Locate and identify every blood parasite.
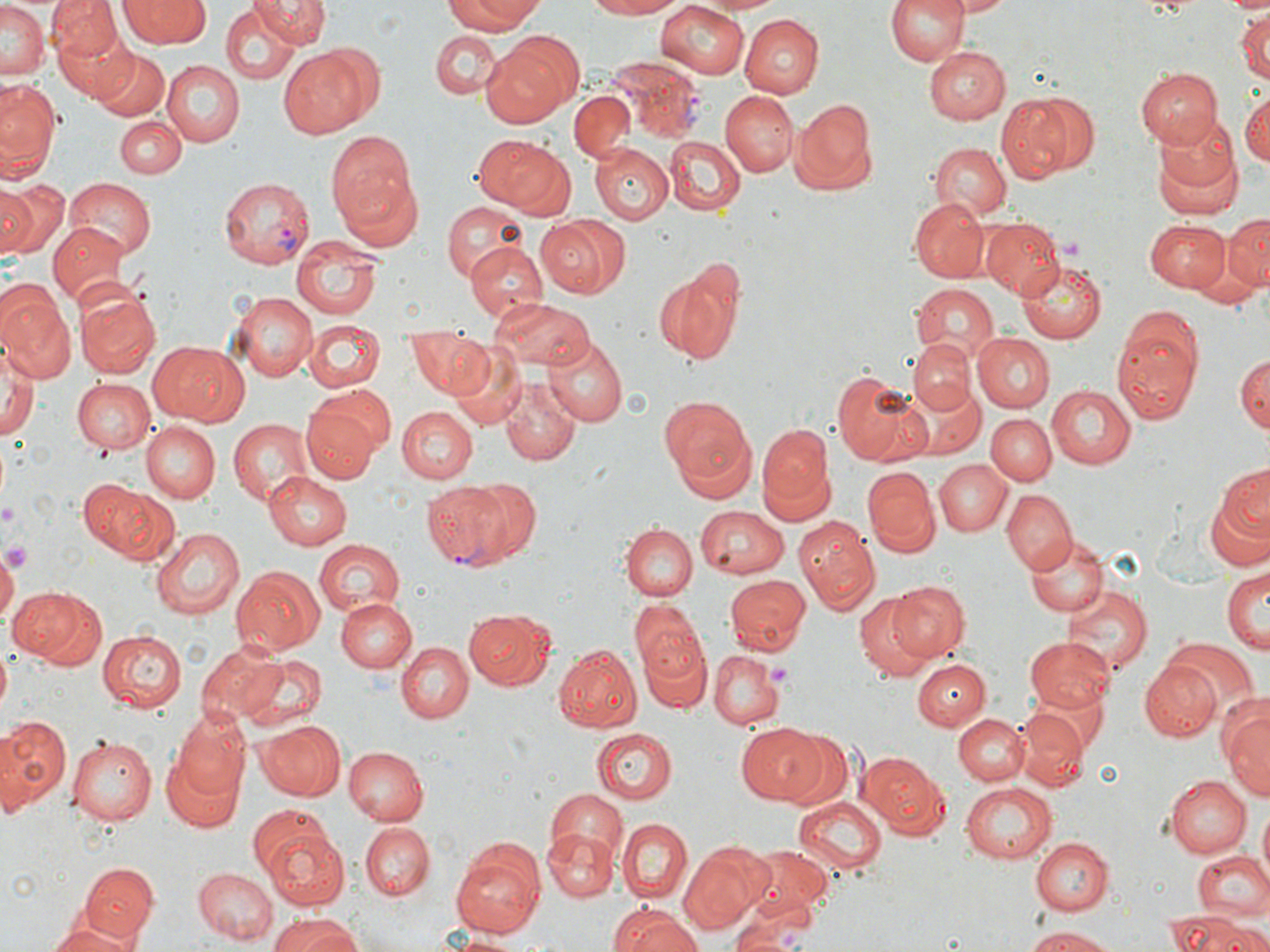

Approximate bounding boxes as named x1/y1/x2/y2 corners in pixels.
Plasmodium vivax-infected red blood cells: (x1=609, y1=55, x2=705, y2=139), (x1=217, y1=176, x2=315, y2=266), (x1=423, y1=479, x2=516, y2=568).
No Plasmodium falciparum, Plasmodium ovale, Plasmodium malariae, Babesia divergens, or Trypanosoma brucei observed.

Summary:
  - Platelet locations: (x1=1056, y1=234, x2=1084, y2=262), (x1=766, y1=663, x2=791, y2=688)
  - Uninfected red blood cell locations: (x1=49, y1=0, x2=125, y2=66), (x1=257, y1=0, x2=328, y2=46), (x1=445, y1=0, x2=544, y2=34), (x1=584, y1=0, x2=686, y2=20), (x1=886, y1=0, x2=969, y2=67), (x1=949, y1=0, x2=1015, y2=16), (x1=119, y1=1, x2=211, y2=47), (x1=655, y1=1, x2=752, y2=79), (x1=1, y1=3, x2=47, y2=81), (x1=221, y1=7, x2=299, y2=85), (x1=892, y1=8, x2=990, y2=109), (x1=1234, y1=9, x2=1270, y2=85), (x1=740, y1=14, x2=823, y2=98), (x1=58, y1=26, x2=137, y2=101), (x1=430, y1=28, x2=502, y2=98), (x1=512, y1=29, x2=585, y2=107), (x1=480, y1=40, x2=574, y2=126), (x1=923, y1=45, x2=1009, y2=124), (x1=278, y1=47, x2=372, y2=138), (x1=94, y1=50, x2=170, y2=120), (x1=162, y1=59, x2=242, y2=147), (x1=1136, y1=68, x2=1222, y2=148), (x1=0, y1=79, x2=61, y2=180), (x1=569, y1=90, x2=637, y2=162), (x1=718, y1=90, x2=796, y2=177), (x1=1239, y1=90, x2=1269, y2=169), (x1=996, y1=94, x2=1080, y2=183), (x1=788, y1=98, x2=876, y2=191), (x1=1151, y1=110, x2=1237, y2=195), (x1=115, y1=117, x2=185, y2=179), (x1=326, y1=131, x2=418, y2=232), (x1=472, y1=134, x2=574, y2=213), (x1=664, y1=136, x2=745, y2=214), (x1=1154, y1=140, x2=1245, y2=223), (x1=931, y1=142, x2=1012, y2=221), (x1=591, y1=143, x2=672, y2=223), (x1=338, y1=171, x2=424, y2=252), (x1=0, y1=178, x2=66, y2=258), (x1=65, y1=178, x2=155, y2=259), (x1=909, y1=198, x2=988, y2=281), (x1=441, y1=201, x2=528, y2=285), (x1=1225, y1=213, x2=1270, y2=291), (x1=534, y1=216, x2=628, y2=298), (x1=980, y1=216, x2=1064, y2=296), (x1=1146, y1=218, x2=1229, y2=293), (x1=47, y1=222, x2=128, y2=305), (x1=990, y1=228, x2=1088, y2=329), (x1=1188, y1=229, x2=1262, y2=301), (x1=291, y1=240, x2=386, y2=318), (x1=466, y1=242, x2=548, y2=319), (x1=1016, y1=259, x2=1105, y2=343), (x1=997, y1=262, x2=1096, y2=397), (x1=653, y1=265, x2=745, y2=363), (x1=909, y1=284, x2=998, y2=359), (x1=0, y1=285, x2=74, y2=383), (x1=73, y1=287, x2=162, y2=379), (x1=230, y1=295, x2=317, y2=380), (x1=493, y1=298, x2=595, y2=373), (x1=1111, y1=311, x2=1201, y2=424), (x1=305, y1=322, x2=383, y2=392), (x1=406, y1=331, x2=489, y2=395), (x1=972, y1=332, x2=1054, y2=411), (x1=545, y1=338, x2=626, y2=425), (x1=908, y1=338, x2=977, y2=416), (x1=152, y1=342, x2=246, y2=426), (x1=0, y1=344, x2=38, y2=441), (x1=451, y1=348, x2=526, y2=429), (x1=1234, y1=350, x2=1269, y2=436), (x1=832, y1=370, x2=928, y2=467), (x1=501, y1=378, x2=580, y2=464), (x1=73, y1=379, x2=155, y2=454), (x1=902, y1=379, x2=986, y2=459), (x1=312, y1=385, x2=395, y2=456), (x1=1046, y1=385, x2=1136, y2=469), (x1=659, y1=397, x2=757, y2=498), (x1=301, y1=403, x2=385, y2=483), (x1=395, y1=406, x2=479, y2=484), (x1=986, y1=413, x2=1057, y2=486), (x1=227, y1=418, x2=313, y2=504), (x1=757, y1=422, x2=833, y2=517), (x1=141, y1=423, x2=220, y2=504), (x1=936, y1=459, x2=1010, y2=537), (x1=1217, y1=464, x2=1269, y2=540), (x1=863, y1=467, x2=940, y2=555), (x1=265, y1=472, x2=353, y2=550), (x1=460, y1=479, x2=544, y2=564), (x1=81, y1=481, x2=180, y2=564), (x1=1002, y1=490, x2=1077, y2=575), (x1=1204, y1=493, x2=1270, y2=573), (x1=694, y1=504, x2=789, y2=579), (x1=792, y1=517, x2=877, y2=611), (x1=619, y1=522, x2=697, y2=602), (x1=151, y1=528, x2=244, y2=618), (x1=1025, y1=534, x2=1108, y2=617), (x1=312, y1=537, x2=405, y2=617), (x1=2, y1=549, x2=19, y2=627), (x1=233, y1=567, x2=325, y2=656), (x1=1221, y1=568, x2=1268, y2=652), (x1=723, y1=574, x2=811, y2=654), (x1=888, y1=581, x2=968, y2=660), (x1=1062, y1=585, x2=1151, y2=675), (x1=10, y1=587, x2=106, y2=669), (x1=335, y1=597, x2=414, y2=674), (x1=854, y1=597, x2=936, y2=682), (x1=631, y1=600, x2=707, y2=686), (x1=464, y1=609, x2=553, y2=690), (x1=98, y1=630, x2=187, y2=711), (x1=638, y1=632, x2=710, y2=713), (x1=1026, y1=637, x2=1114, y2=713), (x1=1164, y1=640, x2=1259, y2=716), (x1=397, y1=641, x2=473, y2=721), (x1=196, y1=644, x2=291, y2=726), (x1=554, y1=645, x2=641, y2=732), (x1=708, y1=650, x2=785, y2=727), (x1=238, y1=654, x2=329, y2=730), (x1=912, y1=658, x2=991, y2=731), (x1=1140, y1=659, x2=1222, y2=739), (x1=1223, y1=704, x2=1269, y2=805), (x1=1016, y1=710, x2=1091, y2=792), (x1=173, y1=712, x2=252, y2=803), (x1=953, y1=713, x2=1028, y2=786), (x1=0, y1=716, x2=71, y2=813), (x1=256, y1=720, x2=345, y2=800), (x1=736, y1=723, x2=829, y2=805), (x1=594, y1=728, x2=676, y2=803), (x1=778, y1=730, x2=855, y2=813), (x1=67, y1=738, x2=156, y2=823), (x1=343, y1=747, x2=428, y2=824), (x1=162, y1=751, x2=242, y2=834), (x1=858, y1=751, x2=948, y2=837), (x1=1167, y1=772, x2=1253, y2=858), (x1=959, y1=783, x2=1058, y2=864), (x1=542, y1=788, x2=628, y2=876), (x1=795, y1=796, x2=887, y2=872), (x1=1256, y1=803, x2=1269, y2=880), (x1=248, y1=804, x2=337, y2=879), (x1=616, y1=817, x2=692, y2=903), (x1=360, y1=824, x2=432, y2=899), (x1=263, y1=828, x2=350, y2=911), (x1=543, y1=828, x2=618, y2=901), (x1=1030, y1=837, x2=1111, y2=914), (x1=452, y1=842, x2=545, y2=935), (x1=678, y1=842, x2=771, y2=933), (x1=739, y1=846, x2=833, y2=920), (x1=1191, y1=850, x2=1270, y2=920), (x1=80, y1=862, x2=158, y2=944), (x1=193, y1=867, x2=278, y2=944), (x1=57, y1=899, x2=146, y2=945), (x1=729, y1=901, x2=815, y2=952), (x1=609, y1=903, x2=701, y2=952), (x1=1162, y1=912, x2=1257, y2=952), (x1=265, y1=914, x2=359, y2=952), (x1=46, y1=919, x2=136, y2=952), (x1=1021, y1=927, x2=1123, y2=950), (x1=438, y1=930, x2=525, y2=950)
  - Slide-level diagnosis: Plasmodium vivax
  - Stain: May-Grünwald-Giemsa
  - Modality: light microscopy
  - Magnification: 1000x
  - Field of view: single
  - Image size: 1270×952 pixels
  - Preparation: thin blood smear